Identify the preparation type.
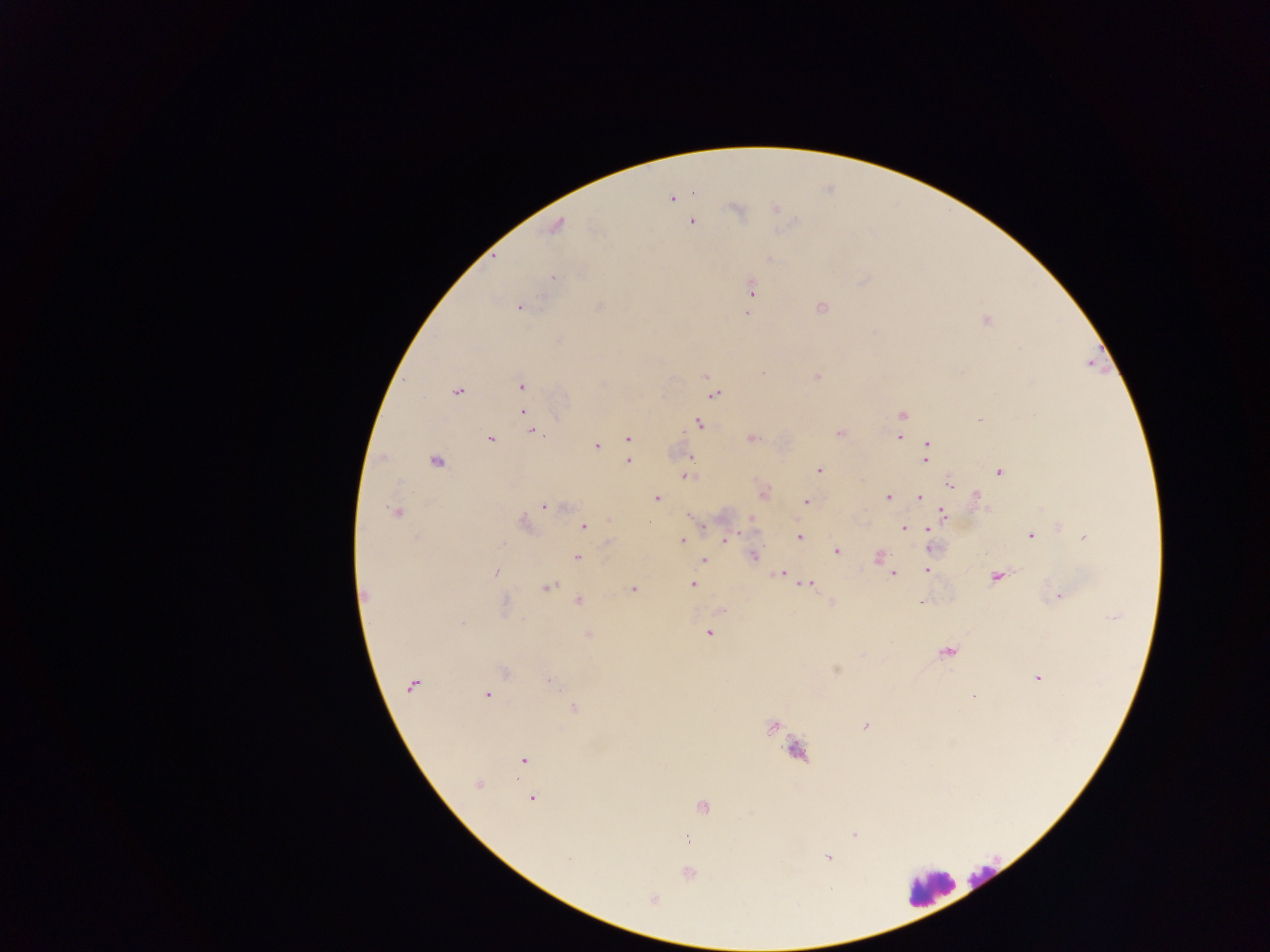
This is a thick smear.

Approximate centers as {x, y} in pixels.
Summary:
  - Leukocyte locations: {796, 751}, {983, 876}, {930, 887}
  - Plasmodium parasite locations: {694, 193}, {671, 199}, {736, 209}, {774, 209}, {691, 221}, {556, 225}, {768, 259}, {553, 278}, {751, 288}, {519, 306}, {820, 306}, {748, 312}, {986, 320}, {705, 376}, {815, 376}, {521, 385}, {456, 391}, {714, 393}, {522, 411}, {901, 415}, {980, 419}, {698, 423}, {532, 430}, {839, 432}, {899, 437}, {489, 438}, {751, 438}, {627, 439}, {927, 445}, {596, 446}, {690, 458}, {924, 459}, {627, 460}, {435, 461}, {818, 470}, {998, 470}, {686, 475}, {951, 485}, {762, 493}, {888, 497}, {919, 497}, {657, 498}, {976, 499}, {804, 501}, {545, 506}, {396, 512}, {943, 514}, {691, 516}, {750, 518}, {608, 521}, {648, 521}, {523, 523}, {583, 526}, {703, 526}, {1059, 526}, {903, 528}, {927, 528}, {1081, 533}, {1030, 535}, {798, 536}, {1085, 536}, {725, 540}, {682, 541}, {930, 550}, {836, 551}, {753, 555}, {878, 556}, {576, 558}, {703, 560}, {928, 563}, {927, 570}, {495, 572}, {779, 573}, {892, 574}, {996, 575}, {808, 583}, {692, 584}, {547, 587}, {633, 590}, {365, 596}, {1058, 596}, {578, 600}, {831, 603}, {504, 604}, {721, 609}, {462, 623}, {709, 632}, {588, 633}, {948, 652}, {836, 671}, {503, 672}, {1037, 677}, {549, 680}, {412, 685}, {486, 694}, {974, 695}, {574, 708}, {772, 726}, {865, 726}, {524, 760}, {478, 784}, {531, 797}, {701, 805}, {853, 834}, {686, 838}, {827, 858}, {687, 873}, {653, 899}
  - Image size: 1270×952 pixels
  - Capture: mobile-phone photograph through a microscope
  - Country: Ghana
  - Field of view: single